Outline each blood parasite and name the species.
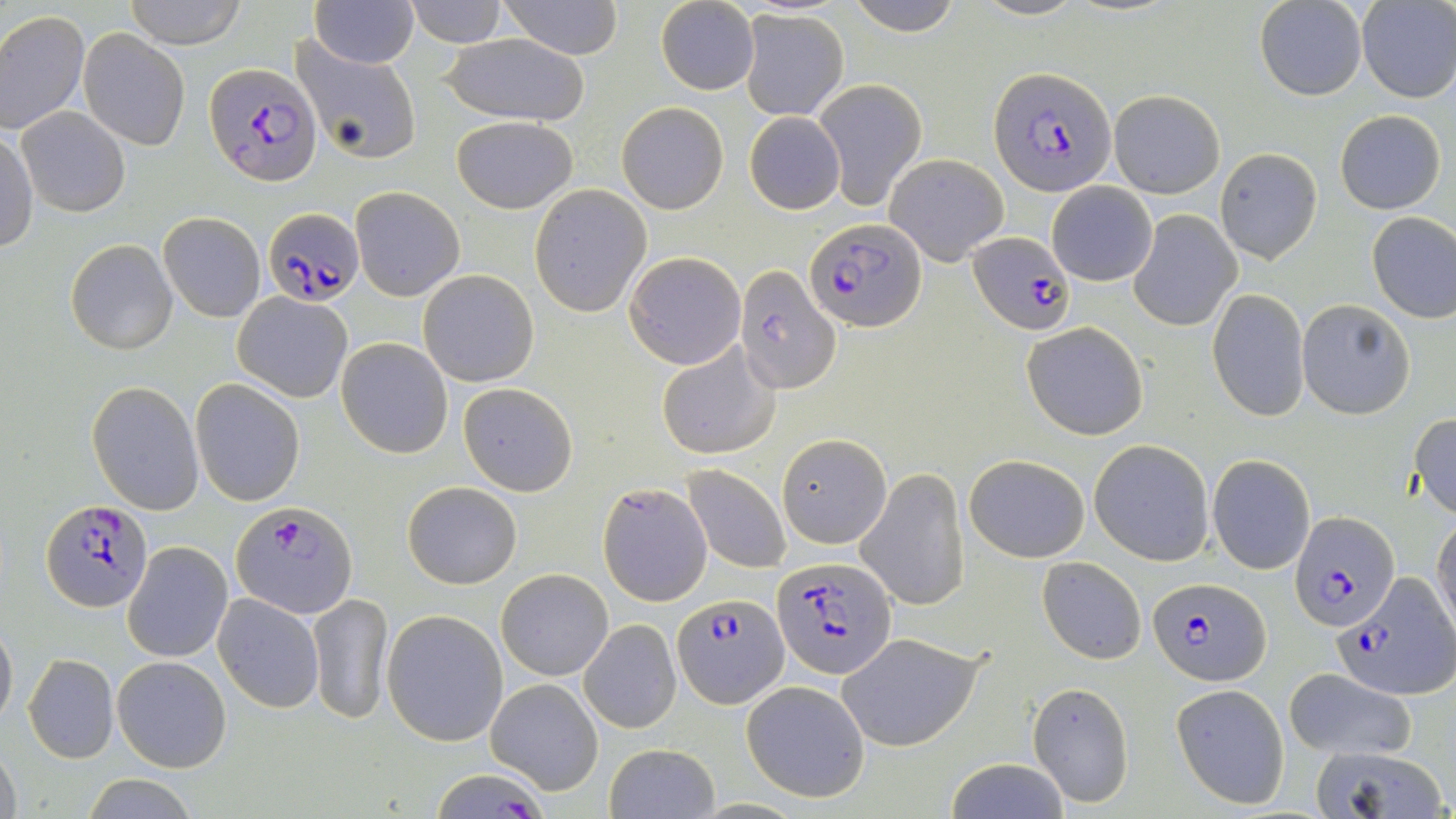

Approximate bounding boxes as (x1, y1, x2, y2) in pixels.
Plasmodium falciparum-infected red blood cells: (206, 62, 321, 186), (990, 67, 1118, 195), (264, 207, 363, 306), (807, 219, 924, 331), (968, 232, 1074, 335), (735, 265, 840, 392), (43, 498, 153, 611), (230, 502, 357, 619), (1289, 508, 1398, 631), (773, 555, 897, 680), (1333, 574, 1454, 699), (1146, 579, 1270, 687), (670, 593, 789, 710), (430, 767, 551, 818).
No Plasmodium ovale, Plasmodium malariae, Plasmodium vivax, Babesia divergens, or Trypanosoma brucei observed.

slide-level diagnosis = Plasmodium falciparum
preparation = thin blood smear
stain = May-Grünwald-Giemsa
field of view = single
modality = optical microscopy
magnification = 1000x
uninfected red blood cell locations = approximate bounding boxes as (x1, y1, x2, y2) in pixels: (125, 0, 246, 49), (311, 0, 417, 68), (403, 0, 507, 47), (500, 0, 623, 58), (845, 0, 965, 34), (972, 0, 1085, 21), (1255, 0, 1366, 100), (1357, 1, 1455, 104), (655, 2, 759, 94), (0, 10, 88, 135), (740, 10, 848, 121), (79, 28, 189, 148), (438, 34, 590, 127), (294, 41, 422, 166), (812, 76, 929, 207), (1110, 90, 1225, 198), (617, 101, 728, 213), (18, 106, 130, 217), (1335, 110, 1446, 214), (744, 111, 846, 214), (450, 115, 578, 214), (0, 130, 38, 253), (1214, 147, 1322, 264), (884, 153, 1009, 265), (1046, 182, 1157, 286), (529, 184, 651, 316), (351, 186, 465, 301), (1128, 209, 1242, 331), (1366, 212, 1456, 323), (158, 213, 265, 321), (66, 239, 177, 354), (624, 251, 747, 370), (419, 269, 538, 387), (1208, 290, 1310, 422), (233, 291, 353, 403), (1297, 300, 1414, 421), (1021, 322, 1149, 440), (337, 338, 453, 458), (656, 341, 782, 460), (190, 378, 305, 505), (86, 381, 204, 514), (457, 383, 578, 496), (1408, 412, 1456, 520), (778, 433, 892, 549), (1089, 439, 1214, 566), (964, 454, 1089, 563), (1206, 455, 1316, 575), (684, 465, 790, 573), (857, 468, 969, 612), (402, 481, 524, 588), (596, 481, 713, 607), (1432, 514, 1456, 637), (122, 541, 233, 663), (1038, 557, 1146, 665), (497, 568, 613, 680), (308, 592, 392, 723), (213, 593, 325, 713), (382, 610, 508, 746), (579, 619, 680, 734), (0, 620, 17, 734), (838, 632, 983, 751), (23, 652, 119, 763), (112, 655, 232, 772), (1283, 668, 1417, 762), (487, 677, 603, 796), (740, 680, 872, 804), (1027, 681, 1136, 808), (1169, 682, 1291, 809), (0, 742, 21, 819), (602, 743, 721, 819), (1306, 743, 1448, 819), (943, 758, 1072, 818), (79, 776, 199, 818)
image size = 1456×819 pixels